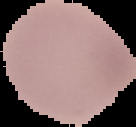
{
  "malaria_status": "uninfected",
  "preparation": "thin blood smear",
  "image_size": "136×127 pixels",
  "image_type": "cell region segmented out of the field of view; surrounding area masked to black"
}